Outline each Plasmodium malariae-infected red blood cell.
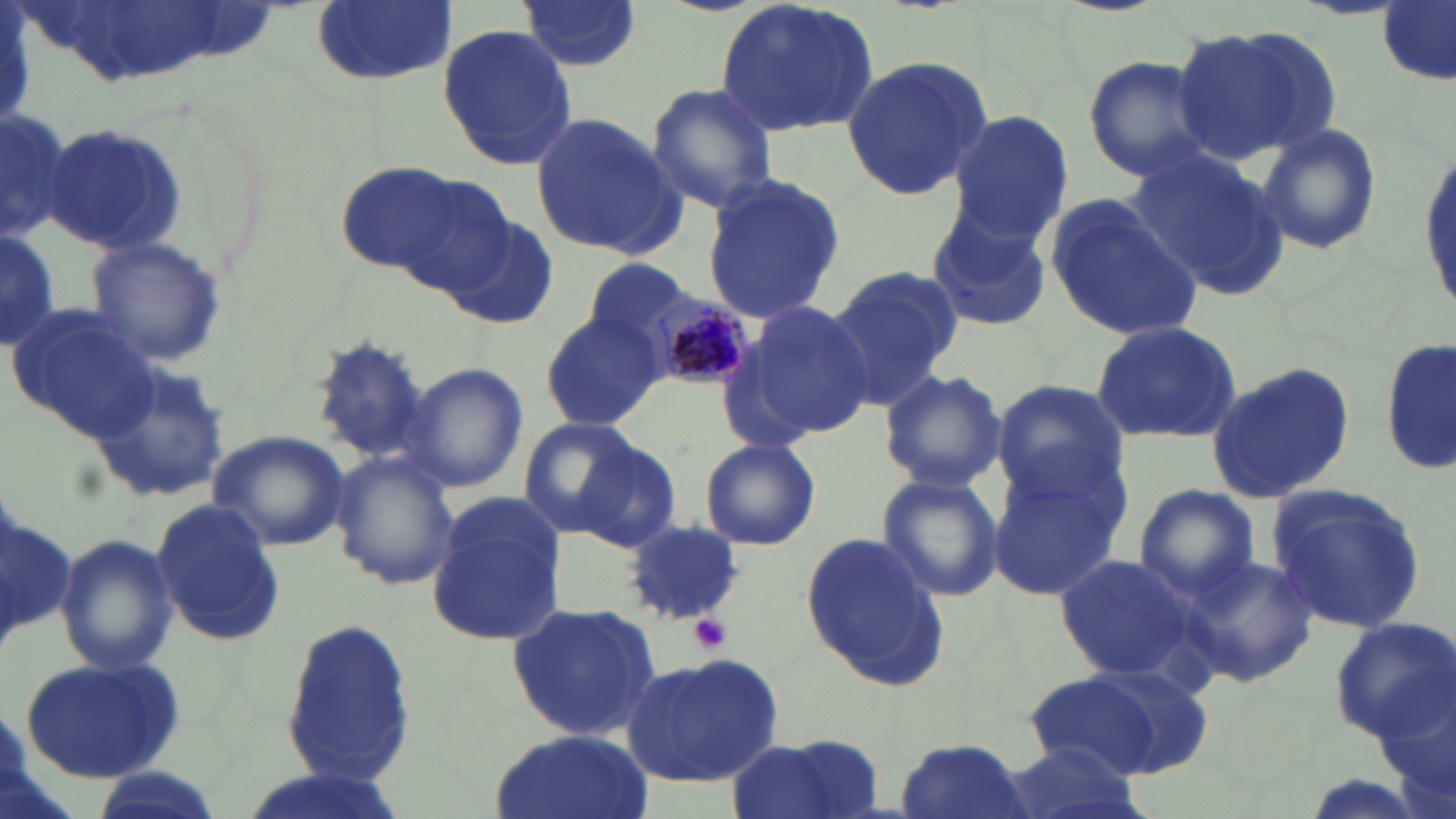

Approximate bounding boxes as [x1, y1, x2, y2] in pixels.
Plasmodium malariae-infected red blood cells: [647, 294, 755, 392].

slide-level diagnosis = Plasmodium malariae
uninfected red blood cell locations = approximate bounding boxes as [x1, y1, x2, y2] in pixels: [310, 0, 457, 87], [713, 0, 880, 140], [516, 1, 641, 73], [1378, 1, 1453, 82], [436, 21, 578, 171], [1173, 23, 1338, 165], [837, 53, 995, 201], [1083, 56, 1216, 181], [646, 83, 780, 213], [1, 105, 71, 246], [530, 111, 683, 259], [947, 111, 1072, 242], [1255, 124, 1383, 255], [39, 126, 188, 253], [1414, 142, 1455, 320], [1131, 147, 1288, 296], [334, 164, 471, 276], [373, 167, 518, 300], [698, 174, 844, 325], [1045, 192, 1205, 342], [924, 206, 1054, 333], [449, 214, 558, 332], [0, 229, 61, 351], [85, 234, 227, 366], [583, 259, 694, 353], [827, 264, 959, 407], [742, 300, 877, 437], [8, 306, 158, 440], [540, 307, 664, 433], [1091, 320, 1245, 445], [309, 336, 435, 465], [1380, 336, 1455, 478], [85, 351, 233, 506], [401, 362, 527, 494], [1204, 363, 1353, 505], [877, 367, 1007, 494], [989, 379, 1128, 505], [517, 417, 641, 536], [207, 430, 350, 550], [569, 438, 683, 551], [699, 438, 822, 551], [330, 451, 460, 592], [985, 464, 1129, 602], [876, 473, 1003, 604], [1265, 483, 1429, 634], [1134, 484, 1259, 603], [151, 498, 286, 646], [427, 498, 564, 647], [619, 518, 745, 623], [54, 530, 179, 676], [801, 530, 949, 691], [1052, 552, 1203, 684], [1179, 553, 1320, 689], [506, 602, 661, 742], [1328, 617, 1456, 743], [282, 619, 415, 788], [624, 652, 783, 787], [17, 658, 186, 785], [1028, 666, 1195, 782], [1376, 666, 1456, 817], [486, 729, 653, 819], [725, 734, 888, 819], [893, 736, 1033, 819], [997, 742, 1145, 819], [85, 767, 223, 819], [229, 769, 414, 819]
modality = light microscopy
magnification = 1000x
field of view = single
white blood cell locations = approximate bounding boxes as [x1, y1, x2, y2] in pixels: [1, 476, 80, 674]
preparation = thin blood film
platelet locations = approximate bounding boxes as [x1, y1, x2, y2] in pixels: [690, 614, 732, 653]
stain = May-Grünwald-Giemsa
image size = 1456×819 pixels